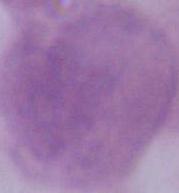
modality = micrograph
identification = red blood cell
magnification = 1000x